Classify this cell by malaria status.
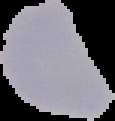
It is parasitized.

preparation = thin blood smear
image type = segmented cell region on a black background
image size = 115×121 pixels